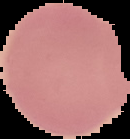
Summary:
  - Image size: 130×139 pixels
  - Result: no Plasmodium parasites detected
  - Preparation: thin blood smear
  - Image type: segmented cell region on a black background